Assess this cell for malaria.
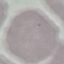
It is uninfected.

stain: Giemsa
capture: smartphone camera at the microscope eyepiece
preparation: thin smear
image_type: cell patch, automatically extracted from a larger field of view and resized to 64 × 64 pixels